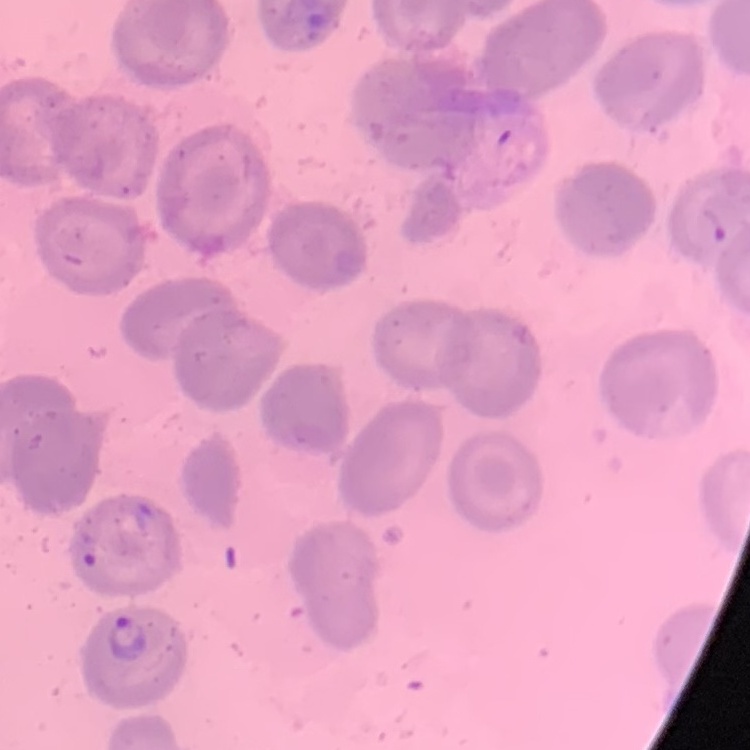
Summary:
  - Red blood cell morphology: no rouleaux formation
  - Preparation: thin blood film
  - Image type: one tile cut from a larger photomicrograph
  - Stain: Field's or Giemsa